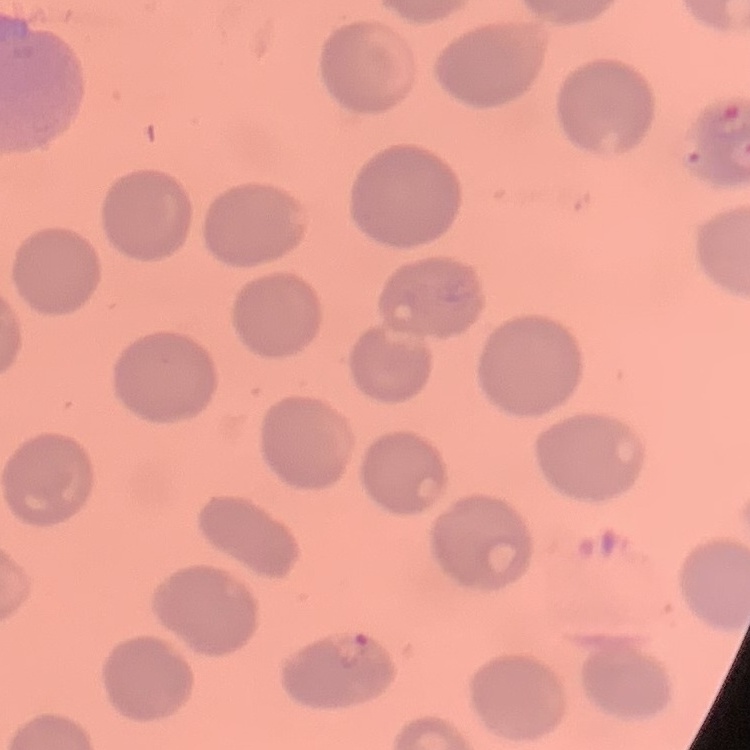

{
  "red_blood_cell_morphology": "no rouleaux formation",
  "image_type": "square crop of a larger photomicrograph",
  "preparation": "thin peripheral smear",
  "stain": "Field's or Giemsa"
}